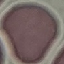

Summary:
  - Result: negative for malaria parasites
  - Stain: Giemsa
  - Image type: automatically extracted cell patch, resized to 64 × 64 pixels
  - Capture: smartphone camera at the microscope eyepiece
  - Preparation: thin smear